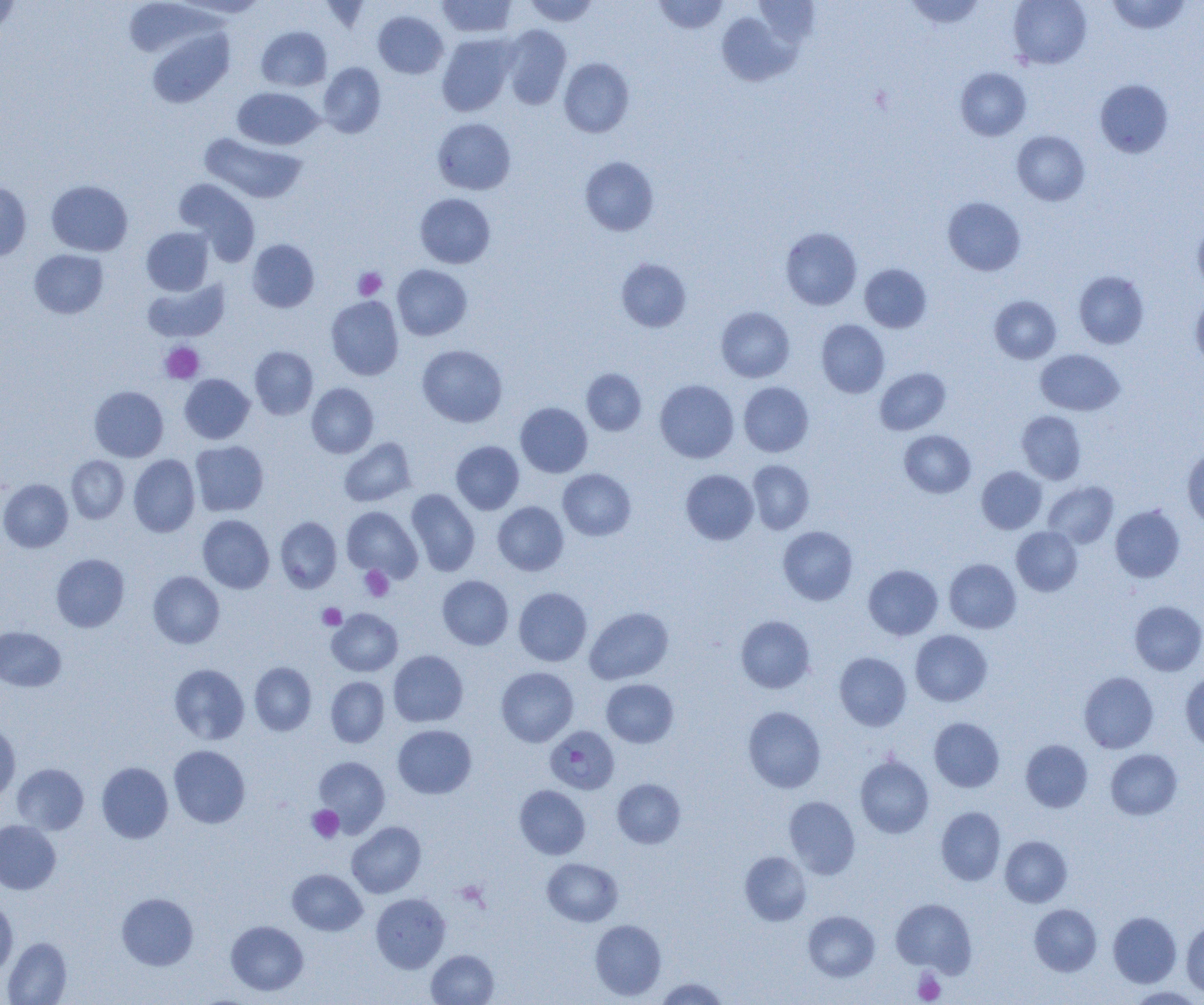

Approximate bounding boxes as (x1, y1, x2, y2) in pixels. Uninfected red blood cell locations: (124, 0, 221, 58), (173, 0, 270, 20), (436, 0, 517, 38), (523, 0, 599, 26), (653, 0, 729, 34), (753, 0, 821, 46), (904, 0, 985, 29), (1008, 0, 1091, 69), (1106, 0, 1192, 34), (0, 1, 20, 39), (373, 11, 448, 79), (716, 11, 799, 86), (501, 25, 571, 109), (257, 27, 331, 91), (147, 28, 234, 108), (436, 33, 517, 116), (559, 58, 634, 137), (318, 62, 386, 138), (955, 67, 1031, 141), (1095, 79, 1174, 157), (232, 87, 324, 150), (433, 118, 515, 195), (1012, 131, 1089, 205), (200, 133, 306, 204), (580, 156, 659, 236), (174, 178, 260, 265), (46, 180, 133, 256), (0, 181, 31, 261), (415, 193, 495, 268), (943, 197, 1026, 276), (1192, 219, 1204, 294), (142, 227, 213, 295), (780, 227, 862, 310), (247, 239, 320, 312), (29, 249, 109, 319), (616, 258, 692, 332), (860, 264, 932, 332), (392, 265, 472, 340), (1074, 271, 1149, 349), (142, 278, 230, 342), (1191, 292, 1204, 369), (326, 295, 404, 380), (989, 295, 1061, 363), (716, 306, 794, 382), (816, 319, 889, 397), (417, 344, 507, 427), (250, 346, 318, 419), (1035, 349, 1125, 416), (875, 368, 950, 435), (581, 369, 646, 435), (179, 374, 255, 444), (655, 379, 739, 463), (739, 381, 814, 457), (306, 383, 379, 458), (89, 386, 168, 461), (515, 402, 592, 478), (1017, 410, 1086, 484), (899, 430, 975, 498), (339, 437, 416, 507), (190, 440, 269, 516), (451, 440, 524, 514), (1182, 448, 1204, 527), (129, 454, 200, 537), (66, 455, 129, 523), (747, 460, 814, 534), (977, 466, 1046, 534), (558, 469, 636, 541), (681, 469, 759, 545), (0, 479, 73, 552), (1043, 481, 1118, 548), (406, 489, 480, 577), (493, 501, 569, 576), (1110, 505, 1185, 582), (342, 506, 422, 582), (197, 514, 274, 593), (275, 516, 342, 593), (778, 526, 858, 605), (1011, 526, 1082, 596), (51, 553, 129, 631), (944, 559, 1021, 633), (863, 564, 943, 639), (148, 571, 225, 648), (437, 575, 514, 649), (514, 587, 592, 666), (1130, 601, 1204, 676), (585, 607, 673, 684), (327, 608, 403, 676), (735, 615, 815, 693), (0, 626, 66, 691), (910, 630, 992, 706), (388, 650, 468, 726), (834, 652, 911, 731), (249, 662, 317, 735), (169, 663, 249, 744), (496, 667, 578, 747), (1180, 669, 1204, 751), (1079, 671, 1158, 753), (326, 676, 389, 747), (601, 679, 678, 747), (743, 706, 825, 793), (929, 717, 1004, 792), (0, 722, 21, 802), (393, 724, 476, 799), (1020, 739, 1093, 812), (169, 745, 250, 828), (1106, 749, 1182, 820), (313, 755, 390, 835), (855, 755, 934, 838), (97, 762, 173, 843), (12, 763, 89, 835), (613, 779, 685, 848), (514, 785, 590, 859), (784, 796, 860, 879), (936, 806, 1006, 885), (0, 820, 61, 894), (347, 821, 426, 897), (1000, 836, 1072, 907), (740, 851, 811, 925), (542, 858, 623, 926), (287, 868, 367, 935), (116, 893, 198, 970), (371, 893, 450, 972), (891, 898, 976, 975), (0, 900, 18, 977), (1029, 904, 1102, 976), (803, 910, 880, 981), (1108, 911, 1181, 987), (589, 919, 666, 1000), (1182, 919, 1204, 998), (226, 920, 308, 996), (2, 937, 72, 1004), (426, 950, 499, 1005), (655, 977, 729, 1005), (1125, 987, 1204, 1004). Platelet locations: (353, 267, 387, 301), (160, 342, 204, 383), (360, 565, 394, 602), (318, 603, 346, 630), (307, 806, 344, 842), (913, 970, 945, 1003). Plasmodium falciparum-infected red blood cell locations: (545, 725, 620, 794). Slide-level diagnosis: Plasmodium falciparum. Optical microscopy. Captured at 1000x magnification. Single field of view. Image is 1204×1005 pixels. Thin blood film.